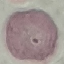
malaria status = uninfected
image type = automatically extracted cell patch, resized to 64 × 64 pixels
stain = Giemsa
preparation = thin smear
capture = smartphone through the microscope eyepiece